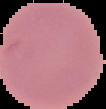

From a thin blood smear. Segmented cell region on a black background. Image is 106×109 pixels. Result: no Plasmodium parasites seen.